Locate every blood parasite and identify its species.
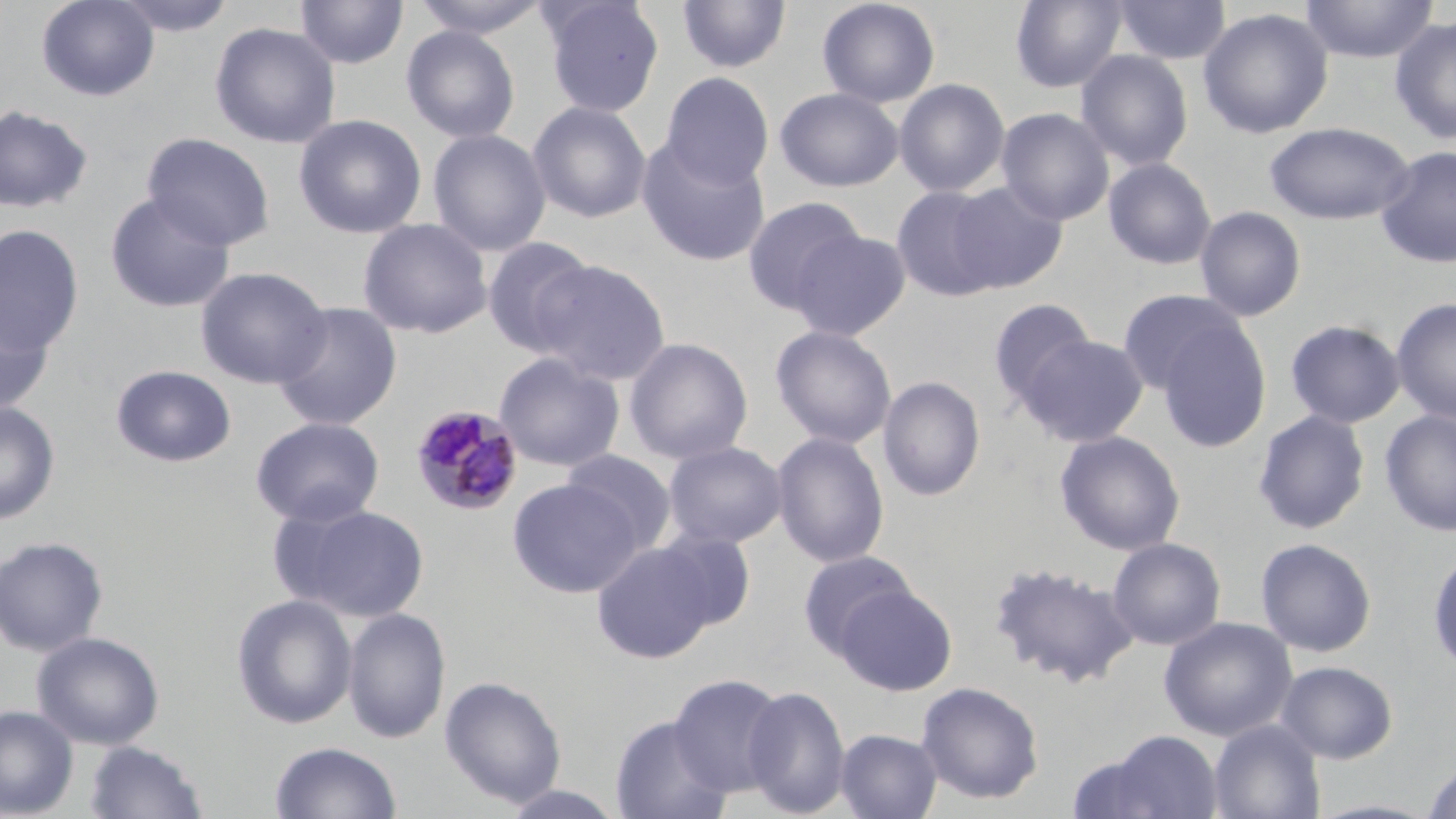

Approximate bounding boxes as named x1/y1/x2/y2 corners in pixels.
Plasmodium malariae-infected red blood cells: (x1=410, y1=404, x2=524, y2=516).
No Plasmodium falciparum, Plasmodium ovale, Plasmodium vivax, Babesia divergens, or Trypanosoma brucei observed.

Uninfected red blood cell locations: (x1=36, y1=0, x2=160, y2=101), (x1=109, y1=0, x2=238, y2=37), (x1=409, y1=0, x2=552, y2=39), (x1=539, y1=0, x2=664, y2=117), (x1=676, y1=0, x2=791, y2=75), (x1=817, y1=0, x2=941, y2=109), (x1=1009, y1=0, x2=1127, y2=93), (x1=1113, y1=0, x2=1231, y2=65), (x1=1299, y1=0, x2=1439, y2=63), (x1=293, y1=1, x2=408, y2=70), (x1=1197, y1=7, x2=1333, y2=139), (x1=1389, y1=15, x2=1456, y2=144), (x1=209, y1=22, x2=341, y2=148), (x1=401, y1=25, x2=520, y2=143), (x1=1076, y1=49, x2=1194, y2=171), (x1=661, y1=72, x2=774, y2=190), (x1=894, y1=78, x2=1011, y2=197), (x1=775, y1=87, x2=903, y2=192), (x1=528, y1=101, x2=652, y2=224), (x1=0, y1=104, x2=94, y2=215), (x1=996, y1=107, x2=1115, y2=226), (x1=293, y1=114, x2=427, y2=238), (x1=1264, y1=121, x2=1415, y2=225), (x1=427, y1=128, x2=551, y2=256), (x1=142, y1=133, x2=275, y2=250), (x1=636, y1=137, x2=771, y2=267), (x1=1376, y1=145, x2=1456, y2=268), (x1=1103, y1=157, x2=1217, y2=270), (x1=946, y1=181, x2=1069, y2=292), (x1=890, y1=185, x2=1007, y2=302), (x1=104, y1=193, x2=236, y2=313), (x1=742, y1=196, x2=867, y2=314), (x1=1194, y1=205, x2=1307, y2=321), (x1=357, y1=218, x2=493, y2=339), (x1=0, y1=224, x2=84, y2=357), (x1=788, y1=228, x2=912, y2=341), (x1=482, y1=237, x2=597, y2=357), (x1=531, y1=259, x2=670, y2=385), (x1=195, y1=266, x2=332, y2=389), (x1=1117, y1=289, x2=1244, y2=397), (x1=0, y1=292, x2=55, y2=416), (x1=1391, y1=297, x2=1456, y2=426), (x1=987, y1=298, x2=1098, y2=410), (x1=271, y1=302, x2=402, y2=431), (x1=1154, y1=319, x2=1272, y2=452), (x1=1285, y1=320, x2=1405, y2=429), (x1=770, y1=325, x2=897, y2=449), (x1=1019, y1=333, x2=1149, y2=446), (x1=624, y1=337, x2=753, y2=465), (x1=493, y1=352, x2=625, y2=472), (x1=111, y1=365, x2=237, y2=468), (x1=878, y1=375, x2=985, y2=502), (x1=0, y1=401, x2=60, y2=525), (x1=1379, y1=409, x2=1456, y2=538), (x1=1252, y1=410, x2=1371, y2=534), (x1=250, y1=417, x2=385, y2=527), (x1=1055, y1=430, x2=1185, y2=555), (x1=771, y1=431, x2=890, y2=568), (x1=662, y1=441, x2=787, y2=549), (x1=559, y1=449, x2=677, y2=556), (x1=507, y1=478, x2=643, y2=598), (x1=281, y1=503, x2=430, y2=622), (x1=651, y1=529, x2=756, y2=632), (x1=0, y1=536, x2=108, y2=656), (x1=1108, y1=537, x2=1226, y2=651), (x1=1255, y1=537, x2=1377, y2=657), (x1=591, y1=541, x2=720, y2=665), (x1=1427, y1=548, x2=1456, y2=675), (x1=798, y1=550, x2=917, y2=659), (x1=988, y1=562, x2=1139, y2=688), (x1=836, y1=584, x2=956, y2=695), (x1=232, y1=593, x2=358, y2=729), (x1=343, y1=607, x2=451, y2=744), (x1=1159, y1=616, x2=1297, y2=741), (x1=32, y1=631, x2=164, y2=750), (x1=1276, y1=660, x2=1398, y2=763), (x1=668, y1=673, x2=786, y2=797), (x1=439, y1=675, x2=567, y2=808), (x1=916, y1=680, x2=1044, y2=804), (x1=741, y1=685, x2=850, y2=817), (x1=0, y1=706, x2=78, y2=817), (x1=609, y1=714, x2=733, y2=819), (x1=1207, y1=719, x2=1325, y2=819), (x1=835, y1=728, x2=942, y2=819), (x1=1084, y1=729, x2=1226, y2=819), (x1=85, y1=740, x2=208, y2=819), (x1=269, y1=740, x2=403, y2=819), (x1=1421, y1=760, x2=1455, y2=819), (x1=498, y1=785, x2=628, y2=819). Slide-level diagnosis: Plasmodium malariae. Single field of view. Light microscopy. 1000x magnification. Thin blood smear. Image is 1456×819 pixels. May-Grünwald-Giemsa stain.